Describe the morphology of the red blood cells.
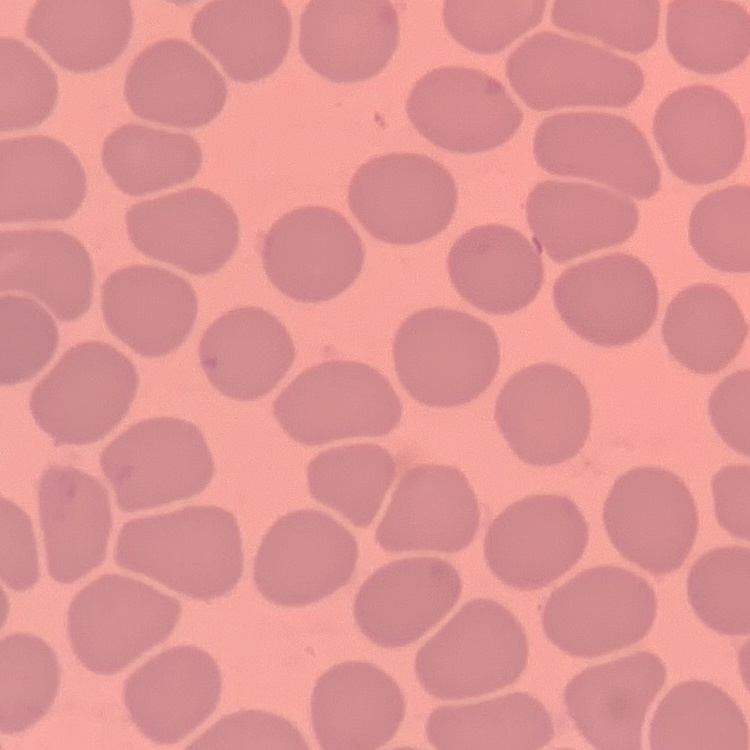
They show no rouleaux formation.

stain = Field's or Giemsa
preparation = thin blood film
image type = square crop of a larger photomicrograph